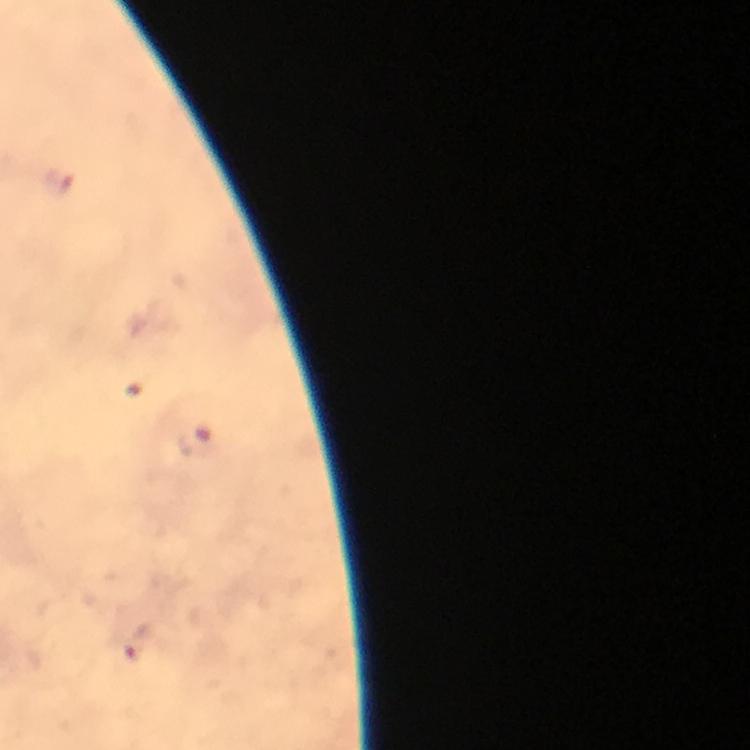

immersion_oil: applied
capture: smartphone camera through the microscope
image_size: 750×750 pixels
magnification: 100x
context: from a malaria diagnostic workup
plasmodium_parasite_locations: 'approximate object centers, in pixels from the top-left corner: (x=57, y=183), (x=196, y=444), (x=140, y=646)'
stain: Giemsa
preparation: thick blood smear
cropped_from: one field of view